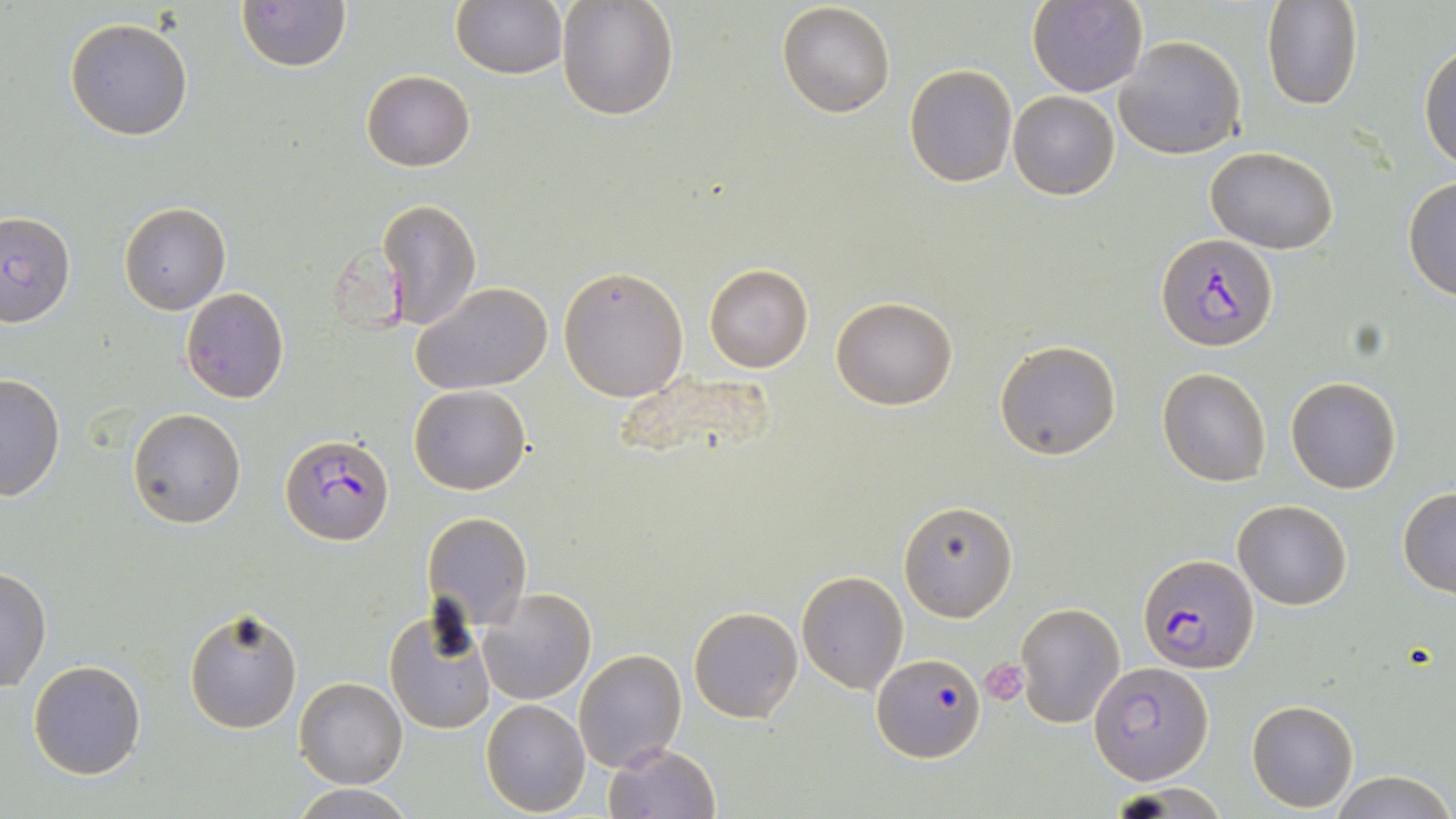
{
  "slide_level_diagnosis": "Plasmodium falciparum",
  "platelet_locations": "approximate bounding boxes as named x1/y1/x2/y2 corners in pixels: (x1=980, y1=658, x2=1028, y2=706)",
  "magnification": "1000x",
  "field_of_view": "one of a larger specimen",
  "modality": "light microscopy",
  "plasmodium_falciparum_infected_red_blood_cell_locations": "approximate bounding boxes as named x1/y1/x2/y2 corners in pixels: (x1=1156, y1=233, x2=1279, y2=351), (x1=279, y1=433, x2=394, y2=548), (x1=1139, y1=554, x2=1258, y2=673), (x1=872, y1=653, x2=984, y2=763), (x1=1092, y1=660, x2=1211, y2=783)",
  "stain": "May-Grünwald-Giemsa",
  "uninfected_red_blood_cell_locations": "approximate bounding boxes as named x1/y1/x2/y2 corners in pixels: (x1=556, y1=0, x2=680, y2=121), (x1=1027, y1=0, x2=1147, y2=97), (x1=1263, y1=0, x2=1365, y2=111), (x1=236, y1=1, x2=351, y2=72), (x1=450, y1=1, x2=567, y2=79), (x1=776, y1=3, x2=895, y2=118), (x1=64, y1=17, x2=194, y2=141), (x1=1115, y1=36, x2=1246, y2=160), (x1=1419, y1=41, x2=1456, y2=172), (x1=903, y1=64, x2=1017, y2=187), (x1=362, y1=70, x2=475, y2=171), (x1=1008, y1=90, x2=1119, y2=200), (x1=1206, y1=146, x2=1340, y2=254), (x1=1402, y1=178, x2=1456, y2=300), (x1=375, y1=197, x2=483, y2=331), (x1=118, y1=202, x2=232, y2=315), (x1=0, y1=210, x2=77, y2=329), (x1=704, y1=263, x2=814, y2=374), (x1=557, y1=264, x2=690, y2=401), (x1=411, y1=281, x2=557, y2=397), (x1=181, y1=287, x2=290, y2=404), (x1=831, y1=296, x2=958, y2=411), (x1=994, y1=339, x2=1122, y2=461), (x1=614, y1=365, x2=781, y2=466), (x1=1156, y1=366, x2=1272, y2=486), (x1=0, y1=373, x2=64, y2=502), (x1=1285, y1=377, x2=1401, y2=494), (x1=408, y1=385, x2=531, y2=496), (x1=128, y1=409, x2=245, y2=529), (x1=1397, y1=488, x2=1456, y2=598), (x1=1232, y1=499, x2=1351, y2=609), (x1=900, y1=500, x2=1017, y2=621), (x1=420, y1=511, x2=533, y2=630), (x1=0, y1=566, x2=52, y2=694), (x1=797, y1=570, x2=908, y2=693), (x1=477, y1=587, x2=598, y2=704), (x1=1017, y1=602, x2=1124, y2=728), (x1=184, y1=605, x2=305, y2=735), (x1=382, y1=605, x2=497, y2=737), (x1=689, y1=606, x2=802, y2=722), (x1=573, y1=648, x2=686, y2=772), (x1=27, y1=659, x2=146, y2=780), (x1=295, y1=676, x2=408, y2=789), (x1=481, y1=699, x2=591, y2=817), (x1=1246, y1=699, x2=1359, y2=812), (x1=602, y1=742, x2=722, y2=819), (x1=1333, y1=771, x2=1453, y2=819), (x1=289, y1=785, x2=418, y2=818)",
  "image_size": "1456×819 pixels",
  "preparation": "thin blood film"
}